Outline each blood parasite and name the species.
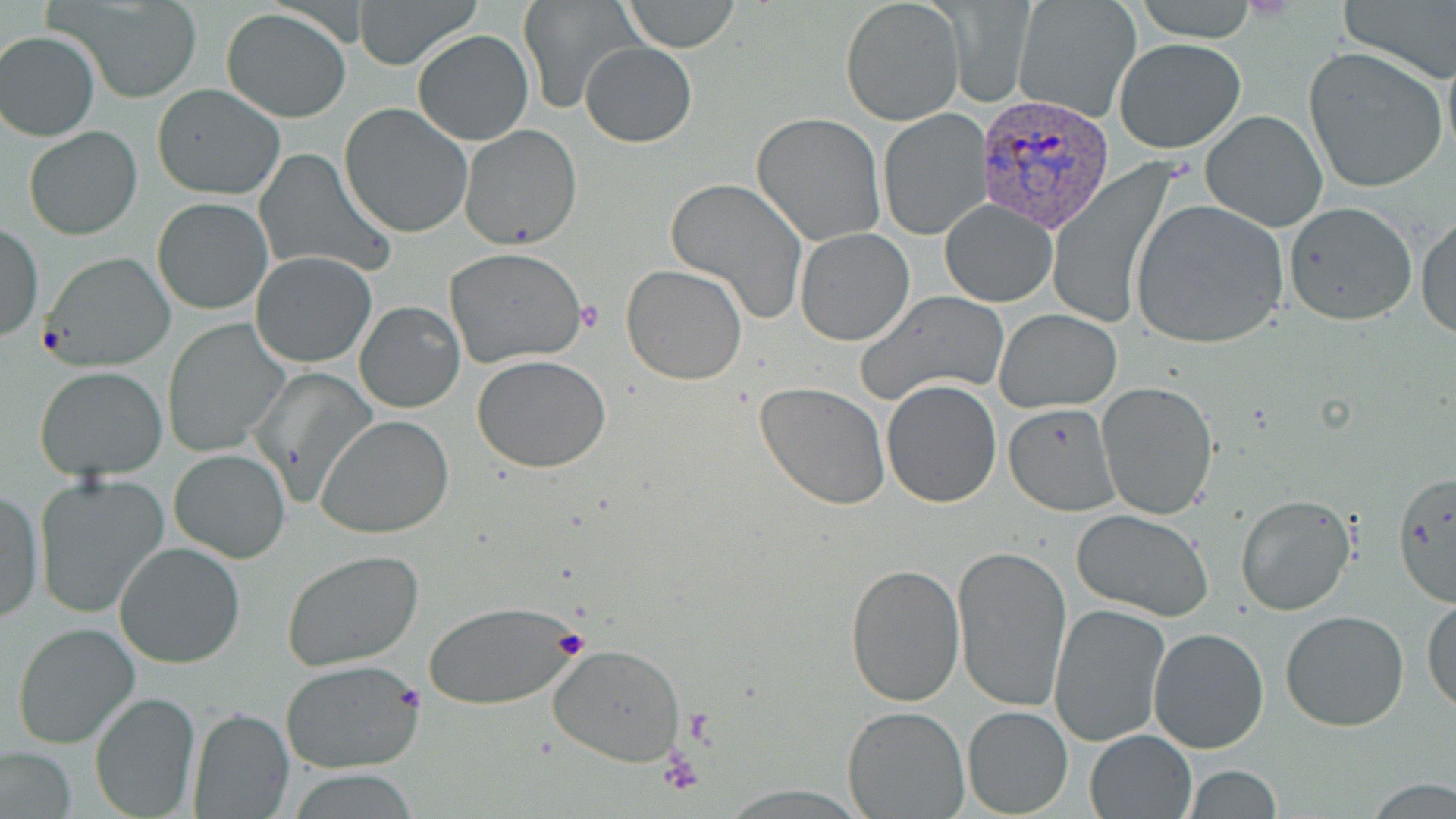
Approximate bounding boxes as named x1/y1/x2/y2 corners in pixels.
Plasmodium vivax-infected red blood cells: (x1=972, y1=92, x2=1118, y2=237).
No Plasmodium falciparum, Plasmodium ovale, Plasmodium malariae, Babesia divergens, or Trypanosoma brucei observed.

{
  "slide_level_diagnosis": "Plasmodium vivax",
  "modality": "optical microscopy",
  "stain": "May-Grünwald-Giemsa",
  "uninfected_red_blood_cell_locations": "approximate bounding boxes as named x1/y1/x2/y2 corners in pixels: (x1=54, y1=0, x2=205, y2=102), (x1=353, y1=0, x2=482, y2=69), (x1=518, y1=0, x2=642, y2=115), (x1=620, y1=0, x2=742, y2=52), (x1=1129, y1=0, x2=1263, y2=41), (x1=1338, y1=0, x2=1456, y2=83), (x1=1012, y1=1, x2=1141, y2=123), (x1=841, y1=2, x2=963, y2=125), (x1=943, y1=5, x2=1034, y2=107), (x1=220, y1=8, x2=352, y2=123), (x1=412, y1=29, x2=534, y2=146), (x1=1, y1=30, x2=100, y2=140), (x1=401, y1=34, x2=556, y2=247), (x1=1113, y1=36, x2=1247, y2=154), (x1=1441, y1=38, x2=1456, y2=167), (x1=580, y1=41, x2=698, y2=147), (x1=1303, y1=45, x2=1448, y2=195), (x1=152, y1=84, x2=285, y2=200), (x1=339, y1=103, x2=473, y2=237), (x1=879, y1=108, x2=994, y2=242), (x1=1200, y1=108, x2=1329, y2=231), (x1=753, y1=112, x2=887, y2=247), (x1=457, y1=124, x2=582, y2=250), (x1=24, y1=125, x2=142, y2=240), (x1=252, y1=149, x2=394, y2=279), (x1=1046, y1=161, x2=1181, y2=330), (x1=666, y1=178, x2=810, y2=324), (x1=152, y1=197, x2=272, y2=315), (x1=939, y1=199, x2=1057, y2=305), (x1=1130, y1=200, x2=1290, y2=348), (x1=1284, y1=200, x2=1418, y2=325), (x1=1416, y1=211, x2=1455, y2=340), (x1=1, y1=223, x2=43, y2=341), (x1=793, y1=227, x2=914, y2=345), (x1=446, y1=247, x2=586, y2=369), (x1=36, y1=252, x2=176, y2=370), (x1=250, y1=252, x2=378, y2=368), (x1=621, y1=265, x2=748, y2=384), (x1=854, y1=290, x2=1010, y2=405), (x1=354, y1=302, x2=464, y2=414), (x1=995, y1=308, x2=1122, y2=412), (x1=162, y1=318, x2=290, y2=457), (x1=472, y1=354, x2=611, y2=473), (x1=35, y1=365, x2=169, y2=480), (x1=254, y1=365, x2=378, y2=509), (x1=880, y1=378, x2=1002, y2=508), (x1=756, y1=381, x2=891, y2=510), (x1=1096, y1=382, x2=1219, y2=520), (x1=1002, y1=402, x2=1121, y2=517), (x1=316, y1=415, x2=456, y2=539), (x1=168, y1=449, x2=290, y2=563), (x1=1392, y1=469, x2=1456, y2=610), (x1=34, y1=473, x2=172, y2=620), (x1=1, y1=489, x2=43, y2=627), (x1=1236, y1=494, x2=1356, y2=616), (x1=1071, y1=510, x2=1214, y2=622), (x1=113, y1=540, x2=245, y2=670), (x1=951, y1=542, x2=1073, y2=713), (x1=281, y1=548, x2=425, y2=671), (x1=844, y1=561, x2=965, y2=707), (x1=1423, y1=595, x2=1455, y2=714), (x1=424, y1=600, x2=580, y2=710), (x1=1048, y1=602, x2=1171, y2=747), (x1=1279, y1=609, x2=1409, y2=733), (x1=11, y1=621, x2=141, y2=750), (x1=1149, y1=628, x2=1269, y2=753), (x1=547, y1=643, x2=687, y2=768), (x1=281, y1=659, x2=425, y2=774), (x1=88, y1=690, x2=203, y2=819), (x1=841, y1=706, x2=969, y2=817), (x1=962, y1=706, x2=1073, y2=817), (x1=188, y1=708, x2=295, y2=819), (x1=1086, y1=730, x2=1196, y2=817), (x1=1, y1=745, x2=76, y2=817), (x1=1182, y1=765, x2=1285, y2=818), (x1=289, y1=772, x2=418, y2=818), (x1=1365, y1=778, x2=1456, y2=817)",
  "preparation": "thin blood film",
  "image_size": "1456×819 pixels",
  "magnification": "1000x",
  "platelet_locations": "approximate bounding boxes as named x1/y1/x2/y2 corners in pixels: (x1=575, y1=297, x2=603, y2=333), (x1=550, y1=627, x2=589, y2=657), (x1=655, y1=745, x2=706, y2=799)",
  "field_of_view": "one of a larger specimen"
}